Name the parasite shown.
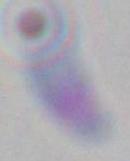

This is Toxoplasma gondii.

Photomicrograph. Captured at 1000x magnification.